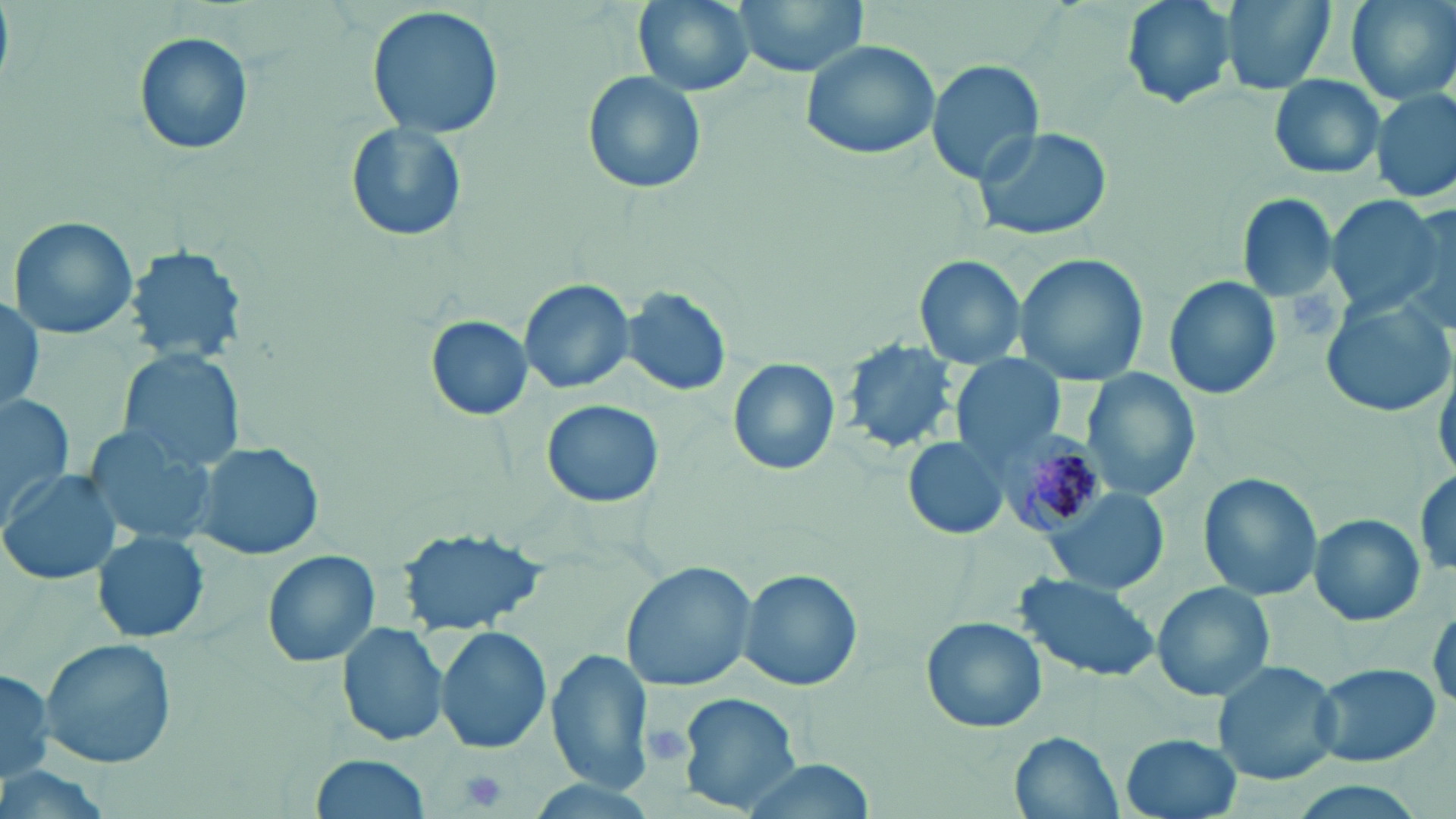
slide-level diagnosis = Plasmodium malariae
stain = May-Grünwald-Giemsa
magnification = 1000x
preparation = thin blood film
image size = 1456×819 pixels
Plasmodium malariae-infected red blood cell locations = approximate bounding boxes as (x1,y1)-(x2,y2) corner pairs in pixels: (994,429)-(1111,539)
field of view = one of a larger specimen
uninfected red blood cell locations = approximate bounding boxes as (x1,y1)-(x2,y2) corner pairs in pixels: (632,0)-(754,97), (733,0)-(869,77), (1118,0)-(1236,111), (1220,0)-(1339,96), (1346,0)-(1455,106), (367,6)-(504,140), (133,32)-(253,156), (799,39)-(940,161), (926,58)-(1045,185), (583,70)-(706,195), (1267,73)-(1386,178), (1371,89)-(1454,203), (345,121)-(469,244), (972,125)-(1115,241), (1236,193)-(1340,301), (1324,194)-(1446,316), (7,214)-(141,342), (122,244)-(248,363), (1013,255)-(1146,388), (915,256)-(1026,368), (1165,276)-(1281,400), (517,279)-(633,395), (622,286)-(731,396), (1,295)-(45,416), (1320,296)-(1454,417), (426,315)-(534,421), (840,341)-(959,457), (120,350)-(244,468), (953,356)-(1062,464), (729,359)-(840,476), (1434,366)-(1455,479), (1080,369)-(1202,503), (0,393)-(75,517), (540,398)-(666,507), (82,425)-(214,549), (904,437)-(1009,541), (189,439)-(325,561), (1,469)-(124,586), (1414,471)-(1453,580), (1199,474)-(1320,603), (1042,489)-(1167,593), (1310,512)-(1426,627), (398,527)-(547,636), (92,529)-(209,643), (261,549)-(380,668), (619,560)-(755,692), (736,568)-(863,692), (1012,574)-(1162,683), (1152,582)-(1275,701), (1429,603)-(1456,710), (920,615)-(1047,733), (338,622)-(449,749), (437,626)-(553,754), (39,639)-(177,768), (548,650)-(654,792), (1211,660)-(1343,787), (1311,661)-(1441,768), (0,668)-(53,783), (679,691)-(801,812), (1010,732)-(1122,818), (1121,733)-(1241,818), (312,754)-(433,819), (734,760)-(879,816)
platelet locations = approximate bounding boxes as (x1,y1)-(x2,y2) corner pairs in pixels: (1292,288)-(1341,337), (641,723)-(693,769), (458,769)-(509,813)
modality = light microscopy